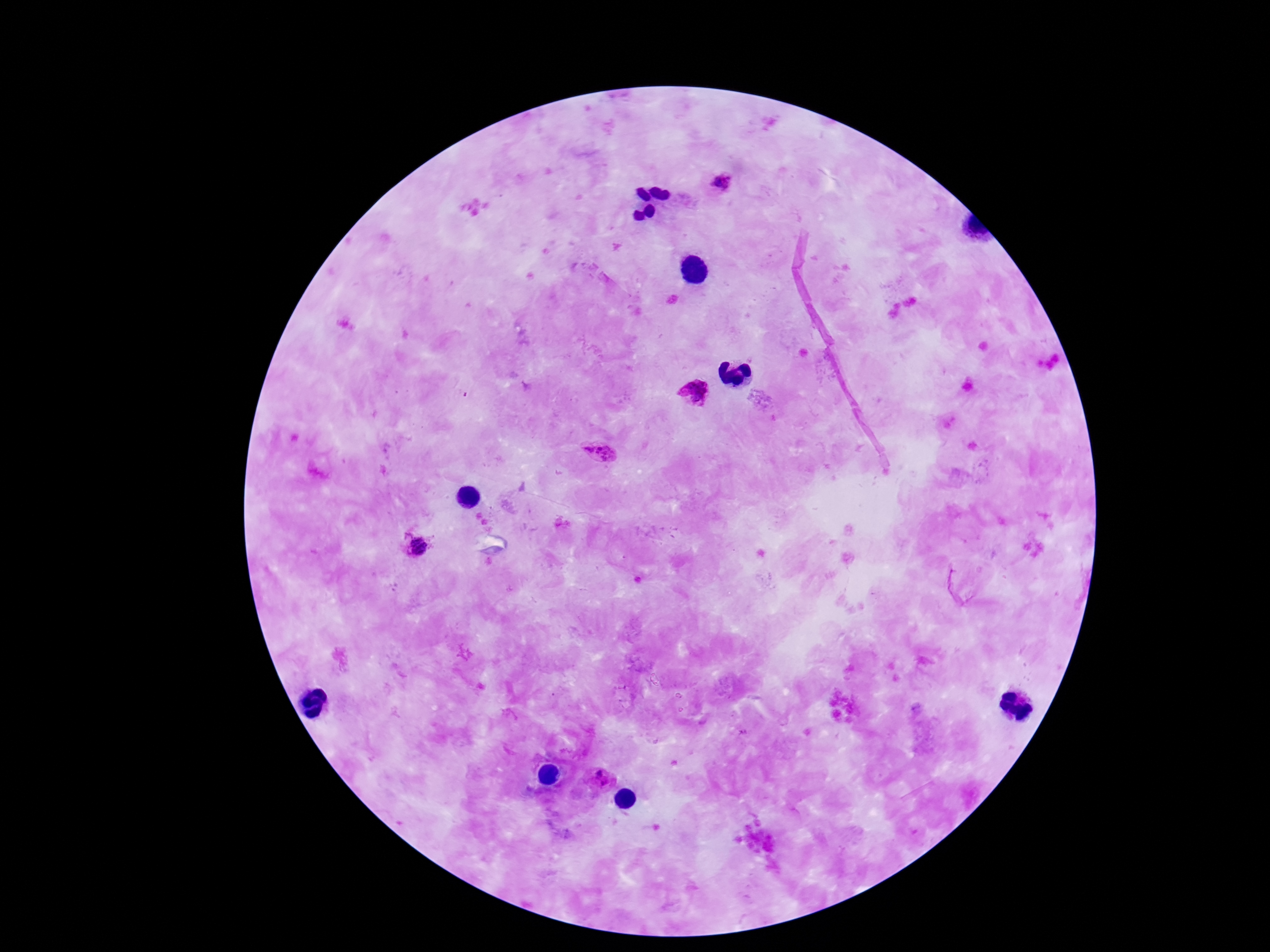

Approximate centers as {x, y} in pixels. Plasmodium parasite locations: {722, 182}, {694, 393}, {599, 452}, {417, 545}, {598, 773}, {607, 785}. One field from this slide. Patient malaria status: infected. Image is 1270×952 pixels. 100x magnification. Thick blood smear. Smartphone photograph taken through the microscope eyepiece. Giemsa-stained preparation.